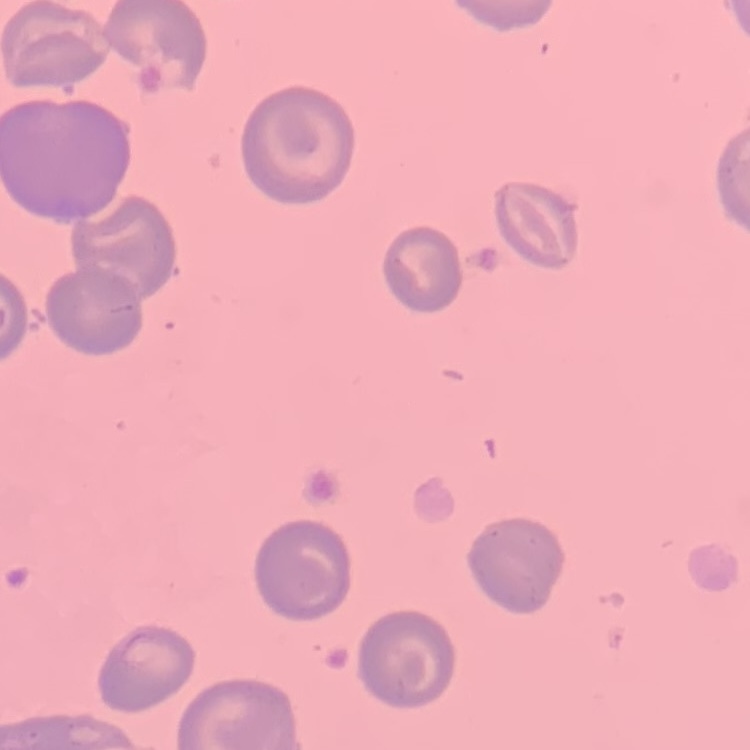

Summary:
  - Erythrocyte morphology: no rouleaux formation
  - Stain: Field's or Giemsa
  - Image type: square crop of a larger photomicrograph
  - Preparation: thin blood smear